Outline each blood parasite and name the species.
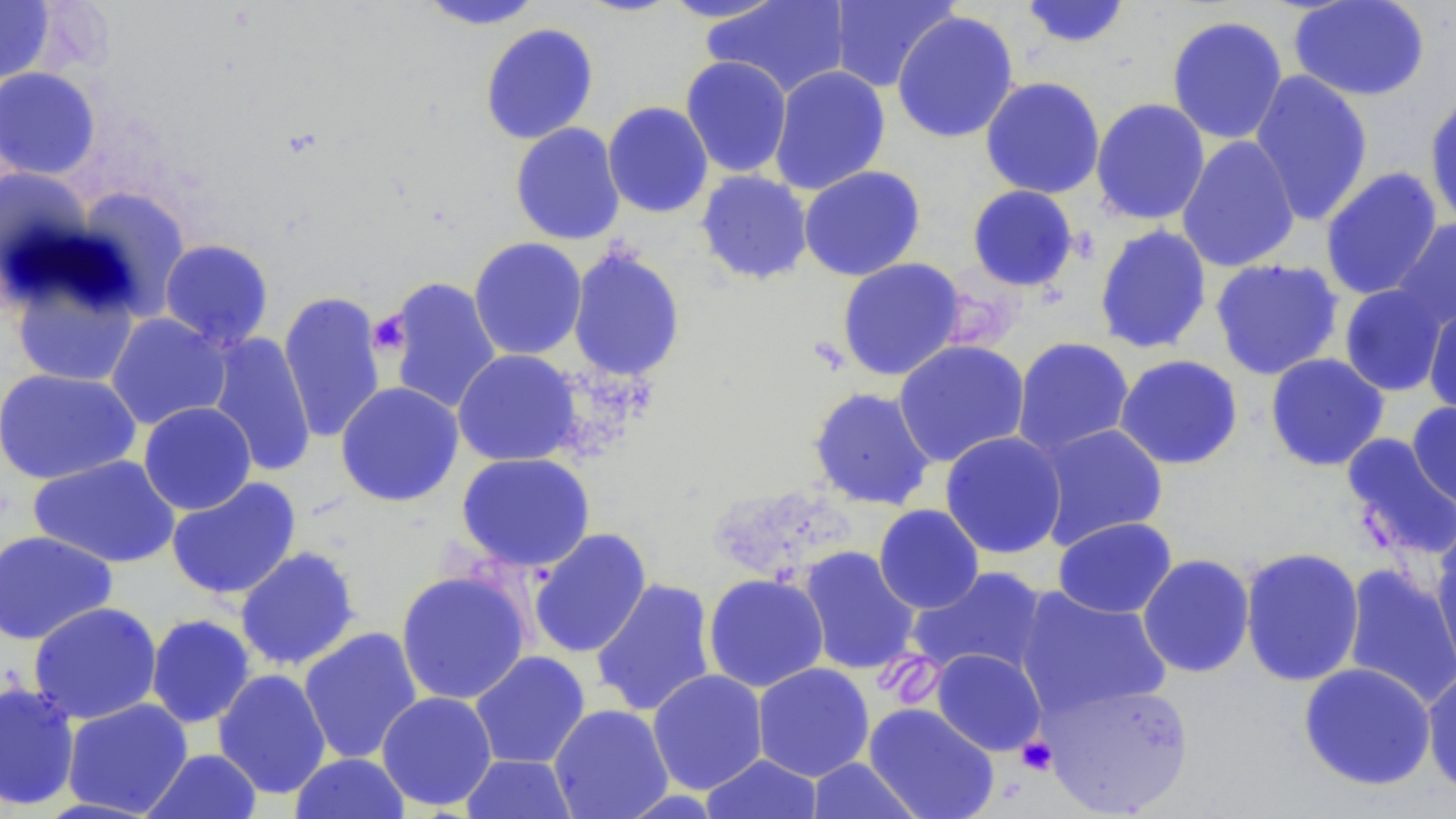
No blood parasites observed.

slide-level diagnosis = no evidence of blood parasites
field of view = single
platelet locations = approximate bounding boxes as (x1, y1, x2, y2) in pixels: (368, 310, 412, 358), (1016, 736, 1057, 776)
stain = May-Grünwald-Giemsa
image size = 1456×819 pixels
modality = optical microscopy
preparation = thin blood smear
magnification = 1000x
uninfected red blood cell locations = approximate bounding boxes as (x1, y1, x2, y2) in pixels: (574, 0, 684, 17), (658, 0, 792, 23), (701, 0, 850, 99), (828, 0, 959, 92), (1019, 0, 1132, 49), (1288, 0, 1431, 101), (0, 1, 55, 86), (416, 1, 546, 30), (891, 10, 1020, 144), (1166, 15, 1289, 145), (480, 23, 599, 144), (680, 55, 793, 178), (769, 65, 891, 195), (0, 67, 101, 181), (1248, 70, 1374, 226), (980, 76, 1106, 199), (1424, 91, 1456, 229), (1090, 97, 1211, 226), (602, 101, 714, 218), (510, 122, 625, 245), (1176, 136, 1301, 273), (798, 165, 926, 281), (1320, 166, 1443, 301), (0, 167, 95, 285), (695, 170, 813, 285), (966, 185, 1079, 292), (72, 186, 192, 318), (1391, 217, 1456, 331), (1093, 224, 1213, 355), (468, 237, 587, 360), (159, 239, 274, 349), (567, 246, 686, 383), (836, 258, 966, 381), (1209, 258, 1344, 380), (8, 263, 142, 388), (383, 276, 503, 415), (1338, 283, 1451, 397), (278, 290, 387, 444), (1422, 303, 1456, 418), (105, 313, 232, 431), (205, 332, 316, 477), (1012, 337, 1135, 458), (893, 339, 1030, 468), (452, 349, 582, 467), (1265, 353, 1390, 472), (1114, 354, 1244, 470), (0, 367, 141, 484), (335, 381, 463, 507), (807, 386, 936, 511), (1406, 400, 1456, 510), (138, 402, 257, 515), (1034, 423, 1169, 550), (940, 431, 1067, 560), (1340, 433, 1456, 562), (456, 452, 595, 572), (28, 454, 181, 568), (166, 477, 302, 600), (873, 504, 985, 614), (1053, 516, 1178, 618), (528, 527, 652, 659), (1430, 528, 1456, 684), (0, 529, 117, 645), (234, 545, 361, 671), (798, 545, 921, 676), (1239, 547, 1365, 687), (1137, 554, 1256, 678), (1342, 562, 1456, 710), (909, 565, 1049, 680), (395, 569, 531, 705), (703, 573, 829, 693), (590, 578, 717, 718), (1014, 586, 1172, 719), (28, 601, 162, 724), (145, 614, 256, 728), (298, 627, 423, 764), (930, 649, 1047, 756), (469, 651, 590, 769), (1298, 662, 1436, 791), (752, 663, 874, 782), (213, 668, 332, 799), (1421, 668, 1456, 799), (647, 669, 768, 795), (1038, 679, 1194, 817), (0, 680, 81, 810), (376, 691, 497, 811), (62, 698, 193, 817), (863, 702, 999, 819), (549, 704, 674, 819), (141, 748, 263, 819), (290, 752, 410, 818), (461, 753, 578, 818), (701, 753, 823, 819), (807, 757, 924, 819)